Assess this cell for malaria.
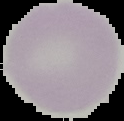

Uninfected.

From a thin blood film. Cell region segmented out of the field of view; the surrounding area is masked to black. Image is 124×121 pixels.